Identify the parasite.
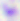
This is Toxoplasma gondii.

magnification = 400x
modality = photomicrograph